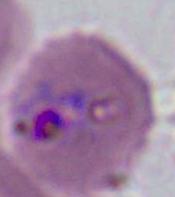 Photomicrograph. A Plasmodium parasite is shown. Captured at either 400x or 1000x magnification.